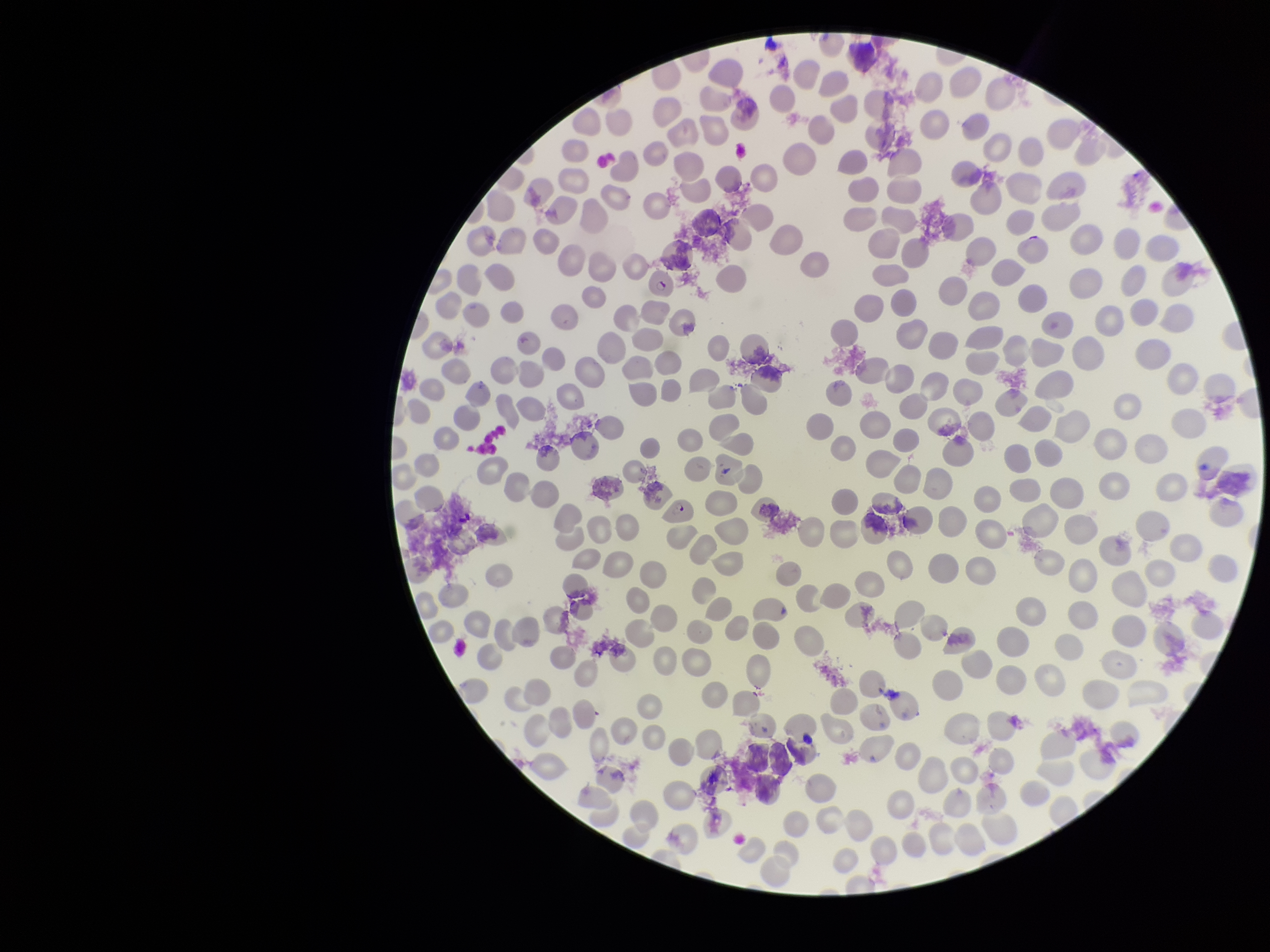
Summary:
  - Stain: Giemsa
  - Red blood cell count: 244
  - Parasitized red blood cells: detected
  - Parasitized red blood cell count: 2
  - Patient malaria status: positive
  - Capture: smartphone photograph through the microscope eyepiece
  - Species reported for this patient: Plasmodium falciparum
  - Field of view: single
  - Image size: 1270×952 pixels
  - Preparation: thin smear